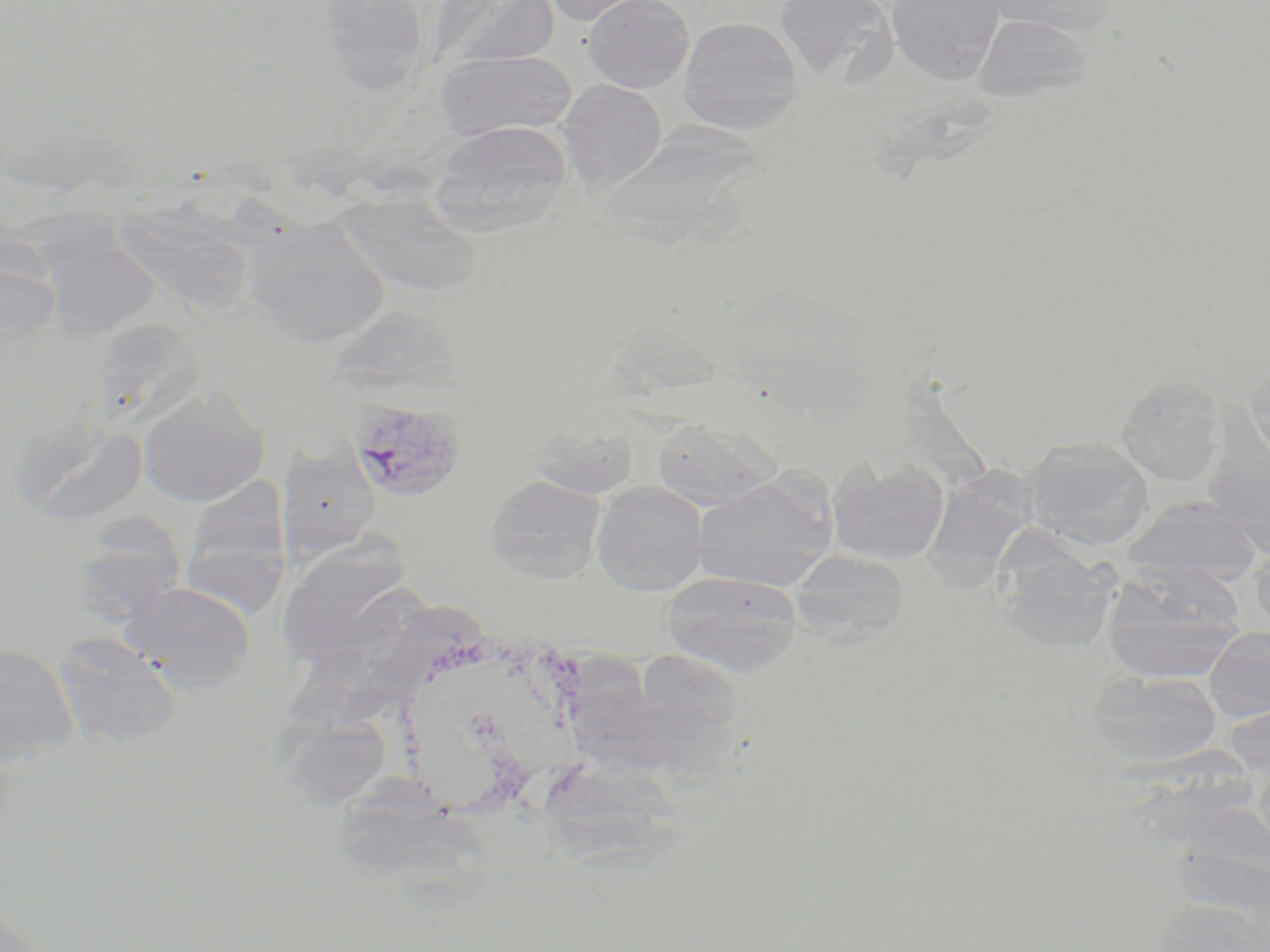
Approximate bounding boxes as [x1, y1, x2, y2] in pixels. Uninfected red blood cell locations: [318, 0, 430, 95], [429, 0, 559, 71], [539, 0, 652, 26], [584, 0, 693, 93], [774, 0, 898, 85], [887, 0, 1005, 83], [991, 0, 1113, 34], [973, 13, 1091, 103], [679, 17, 803, 134], [436, 49, 577, 139], [558, 79, 667, 192], [429, 120, 572, 236], [602, 121, 770, 249], [333, 193, 483, 297], [30, 204, 165, 338], [114, 204, 259, 316], [245, 217, 389, 349], [0, 253, 61, 354], [328, 304, 462, 397], [94, 335, 208, 427], [1245, 360, 1270, 469], [1116, 375, 1225, 486], [138, 386, 270, 507], [11, 413, 149, 528], [652, 417, 780, 510], [528, 421, 639, 501], [1022, 436, 1154, 550], [277, 448, 381, 560], [827, 457, 950, 564], [931, 461, 1039, 591], [691, 473, 837, 591], [485, 474, 605, 583], [181, 476, 293, 613], [591, 480, 710, 596], [1122, 496, 1262, 588], [73, 514, 188, 623], [278, 540, 414, 666], [1249, 542, 1270, 636], [998, 548, 1118, 654], [789, 549, 909, 644], [1102, 562, 1245, 683], [659, 570, 803, 676], [121, 580, 256, 692], [1203, 626, 1270, 722], [52, 632, 182, 749], [0, 644, 79, 763], [560, 649, 676, 783], [633, 649, 744, 741], [1085, 670, 1223, 768], [271, 705, 393, 809], [544, 749, 690, 881], [343, 774, 492, 906], [1147, 897, 1270, 952], [0, 901, 52, 952]. Plasmodium vivax-infected red blood cell locations: [347, 398, 466, 504]. Slide-level diagnosis: Plasmodium vivax. May-Grünwald-Giemsa stain. Thin blood film. Optical microscopy. One field of a larger specimen. 1000x magnification. Image is 1270×952 pixels.